Assess this cell for malaria.
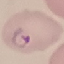
It is parasitized.

Summary:
  - Stain: Giemsa
  - Image type: automatically extracted cell patch, resized to 64 × 64 pixels
  - Capture: smartphone through the microscope eyepiece
  - Preparation: thin blood film